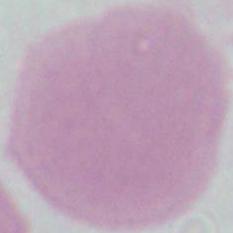
modality = micrograph
identification = red blood cell
magnification = 1000x